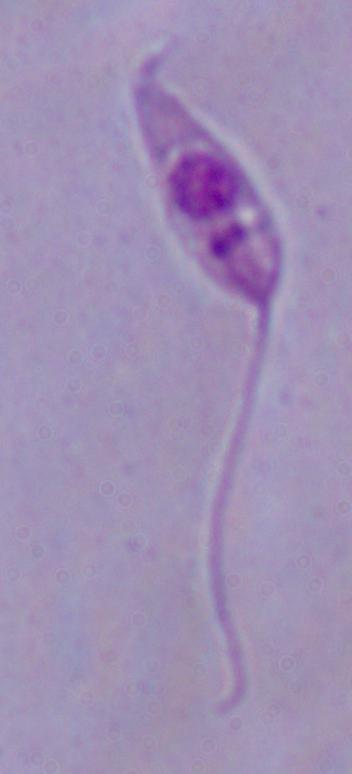
Summary:
  - Magnification: 1000x
  - Identification: Leishmania
  - Modality: micrograph